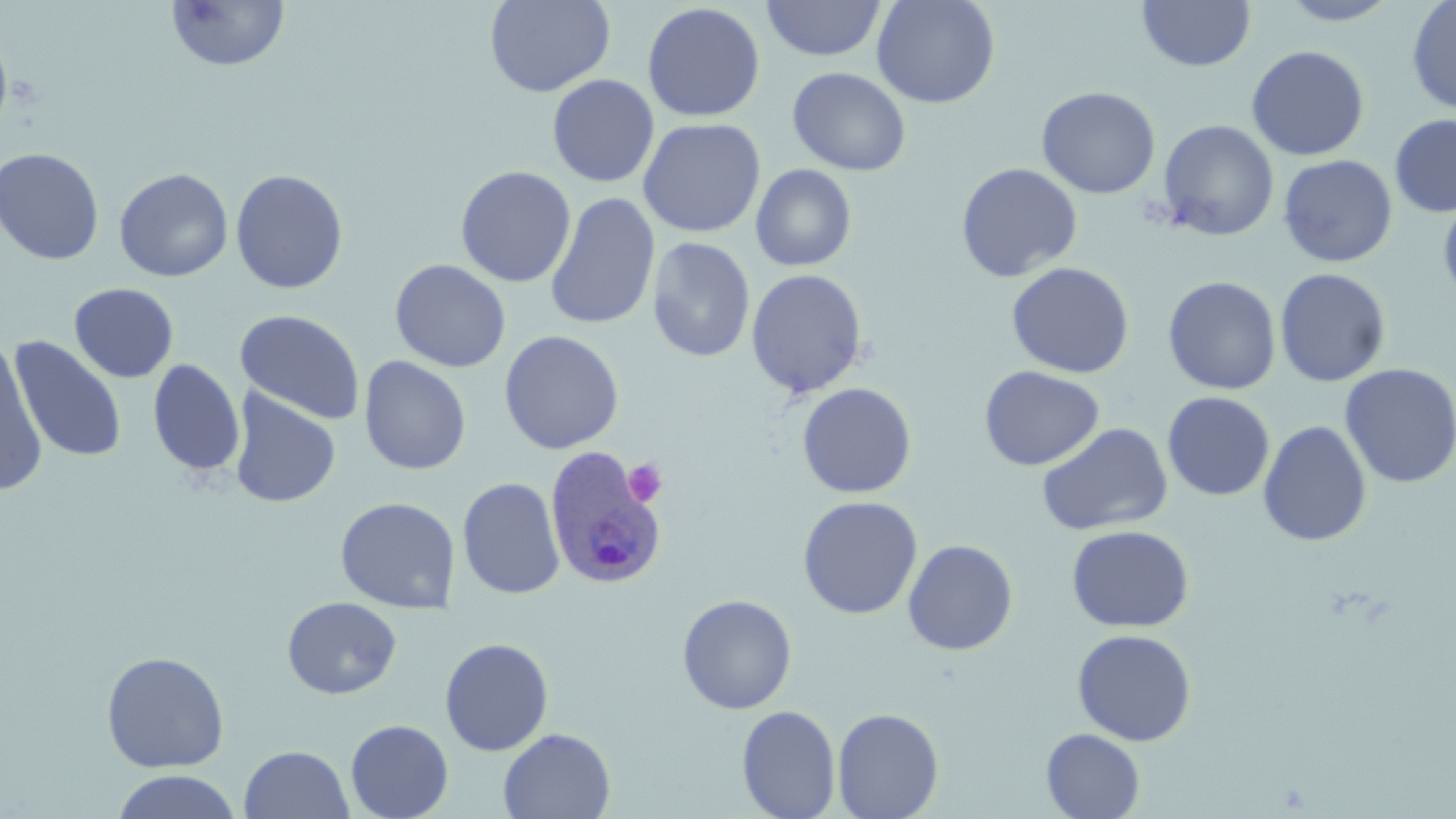

Summary:
  - Coordinate format: approximate bounding boxes as (x1, y1, x2, y2) in pixels
  - Uninfected red blood cell locations: (166, 0, 290, 73), (484, 0, 615, 97), (762, 0, 886, 62), (871, 0, 1001, 109), (1137, 0, 1256, 71), (1276, 1, 1401, 25), (1406, 1, 1456, 115), (642, 3, 766, 123), (0, 30, 12, 135), (1247, 45, 1370, 161), (787, 67, 912, 176), (547, 74, 659, 188), (1036, 86, 1161, 199), (1390, 114, 1456, 218), (638, 117, 766, 238), (1157, 119, 1279, 241), (0, 148, 104, 265), (1278, 154, 1397, 267), (956, 162, 1083, 282), (750, 164, 857, 271), (455, 165, 576, 288), (114, 167, 234, 282), (230, 169, 348, 294), (1438, 191, 1456, 311), (545, 193, 661, 330), (647, 237, 755, 362), (390, 259, 511, 372), (1006, 262, 1135, 378), (746, 268, 867, 398), (1274, 268, 1391, 387), (1163, 276, 1281, 394), (69, 282, 179, 383), (234, 309, 365, 425), (499, 330, 624, 454), (8, 336, 127, 463), (0, 337, 48, 497), (358, 355, 471, 475), (147, 358, 245, 477), (1339, 363, 1455, 488), (979, 365, 1104, 471), (796, 382, 917, 499), (229, 388, 341, 508), (1162, 391, 1275, 501), (1258, 420, 1372, 547), (1037, 422, 1173, 537), (457, 477, 565, 600), (335, 496, 460, 614), (798, 496, 922, 619), (1066, 525, 1194, 632), (903, 539, 1019, 655), (677, 594, 797, 715), (282, 596, 402, 699), (1072, 629, 1197, 746), (439, 637, 554, 756), (101, 650, 230, 773), (736, 704, 841, 819), (832, 707, 944, 819), (345, 719, 454, 819), (498, 728, 616, 818), (1041, 728, 1145, 818), (239, 745, 353, 819), (110, 769, 242, 819)
  - Plasmodium ovale-infected red blood cell locations: (543, 446, 667, 589)
  - Platelet locations: (623, 458, 668, 507)
  - Slide-level diagnosis: Plasmodium ovale
  - Modality: light microscopy
  - Stain: May-Grünwald-Giemsa
  - Preparation: thin blood film
  - Field of view: one of a larger specimen
  - Magnification: 1000x
  - Image size: 1456×819 pixels